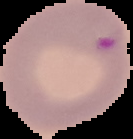

malaria_status: parasitized
image_type: segmented cell region with the area outside set to black
image_size: 133×139 pixels
preparation: thin blood smear